Locate every blood parasite and identify its species.
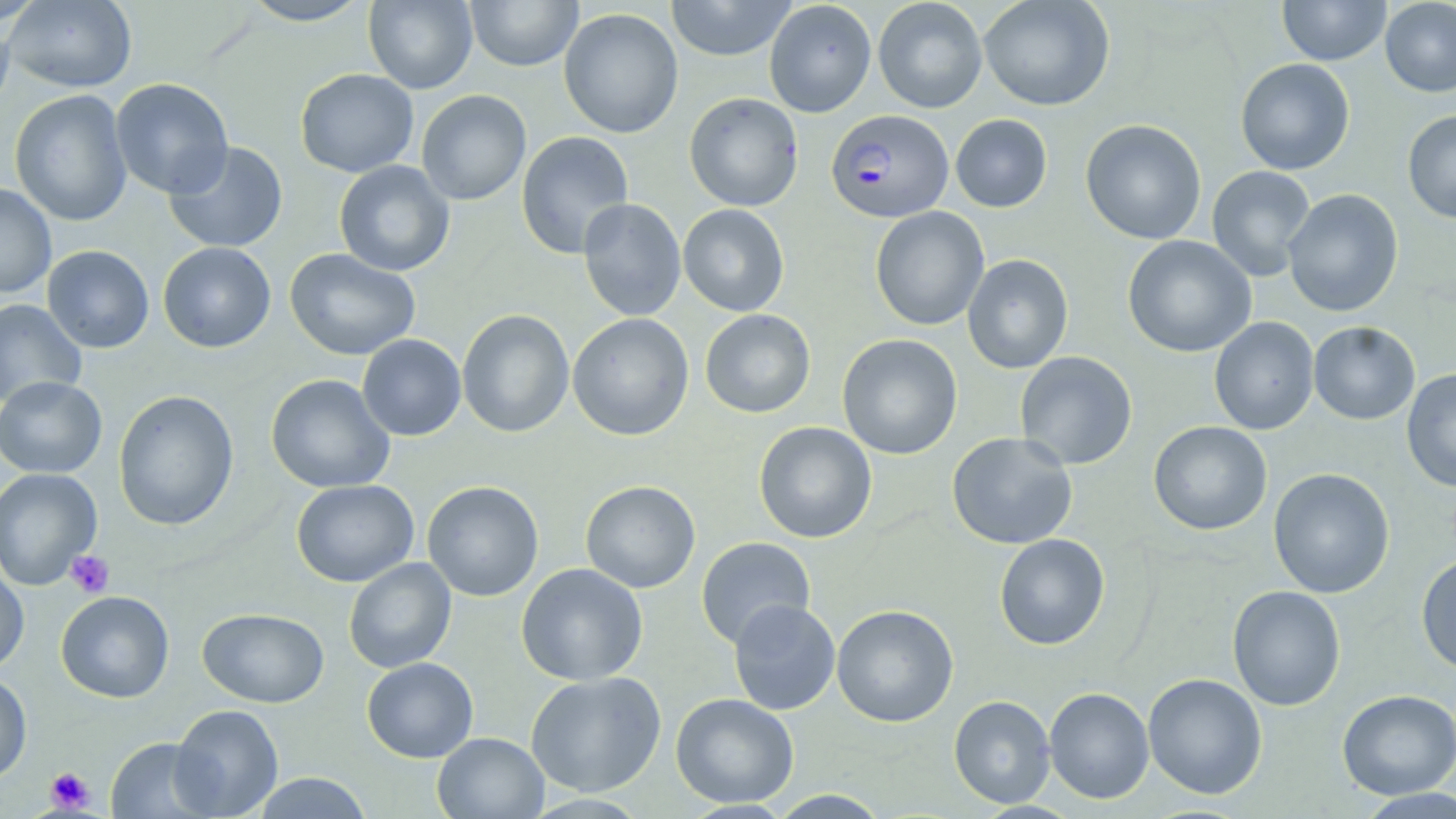

Approximate bounding boxes as named x1/y1/x2/y2 corners in pixels.
Plasmodium falciparum-infected red blood cells: (x1=825, y1=110, x2=953, y2=223).
No Plasmodium ovale, Plasmodium malariae, Plasmodium vivax, Babesia divergens, or Trypanosoma brucei observed.

Platelet locations: (x1=65, y1=550, x2=114, y2=598), (x1=45, y1=766, x2=95, y2=812). Uninfected red blood cell locations: (x1=3, y1=0, x2=137, y2=93), (x1=238, y1=0, x2=373, y2=26), (x1=465, y1=0, x2=583, y2=72), (x1=665, y1=0, x2=798, y2=61), (x1=764, y1=0, x2=877, y2=117), (x1=873, y1=0, x2=988, y2=113), (x1=978, y1=0, x2=1115, y2=111), (x1=1278, y1=0, x2=1391, y2=66), (x1=1380, y1=0, x2=1456, y2=97), (x1=0, y1=1, x2=47, y2=27), (x1=363, y1=1, x2=478, y2=94), (x1=558, y1=8, x2=684, y2=139), (x1=0, y1=13, x2=15, y2=123), (x1=1235, y1=58, x2=1355, y2=175), (x1=295, y1=68, x2=419, y2=178), (x1=110, y1=78, x2=234, y2=199), (x1=9, y1=90, x2=132, y2=227), (x1=416, y1=90, x2=531, y2=205), (x1=683, y1=92, x2=803, y2=211), (x1=1402, y1=110, x2=1456, y2=224), (x1=951, y1=114, x2=1052, y2=213), (x1=1080, y1=118, x2=1207, y2=244), (x1=516, y1=131, x2=634, y2=259), (x1=163, y1=140, x2=288, y2=253), (x1=334, y1=160, x2=455, y2=277), (x1=1207, y1=165, x2=1316, y2=281), (x1=0, y1=183, x2=57, y2=299), (x1=1283, y1=188, x2=1404, y2=317), (x1=577, y1=198, x2=687, y2=321), (x1=677, y1=203, x2=789, y2=317), (x1=870, y1=206, x2=989, y2=331), (x1=1122, y1=235, x2=1256, y2=358), (x1=157, y1=242, x2=276, y2=352), (x1=42, y1=245, x2=154, y2=353), (x1=284, y1=248, x2=421, y2=361), (x1=962, y1=254, x2=1073, y2=374), (x1=0, y1=298, x2=87, y2=408), (x1=457, y1=309, x2=575, y2=438), (x1=700, y1=309, x2=815, y2=418), (x1=568, y1=313, x2=694, y2=441), (x1=1209, y1=317, x2=1320, y2=435), (x1=1308, y1=321, x2=1420, y2=424), (x1=357, y1=334, x2=467, y2=441), (x1=836, y1=334, x2=963, y2=459), (x1=1015, y1=351, x2=1138, y2=470), (x1=1402, y1=368, x2=1456, y2=492), (x1=265, y1=373, x2=395, y2=493), (x1=0, y1=376, x2=107, y2=478), (x1=113, y1=390, x2=239, y2=531), (x1=1148, y1=420, x2=1273, y2=536), (x1=753, y1=421, x2=877, y2=543), (x1=947, y1=432, x2=1078, y2=550), (x1=0, y1=467, x2=102, y2=591), (x1=1268, y1=468, x2=1395, y2=598), (x1=291, y1=479, x2=419, y2=587), (x1=580, y1=480, x2=701, y2=593), (x1=422, y1=481, x2=544, y2=601), (x1=994, y1=534, x2=1110, y2=650), (x1=696, y1=536, x2=816, y2=648), (x1=1416, y1=553, x2=1456, y2=674), (x1=343, y1=558, x2=456, y2=673), (x1=0, y1=562, x2=29, y2=675), (x1=516, y1=563, x2=648, y2=686), (x1=1227, y1=585, x2=1346, y2=711), (x1=55, y1=591, x2=174, y2=703), (x1=728, y1=599, x2=841, y2=715), (x1=831, y1=604, x2=959, y2=727), (x1=197, y1=608, x2=329, y2=708), (x1=361, y1=657, x2=478, y2=763), (x1=525, y1=671, x2=667, y2=797), (x1=0, y1=673, x2=33, y2=784), (x1=1142, y1=673, x2=1268, y2=799), (x1=1044, y1=686, x2=1154, y2=803), (x1=1336, y1=689, x2=1456, y2=799), (x1=671, y1=692, x2=799, y2=808), (x1=948, y1=695, x2=1055, y2=808), (x1=169, y1=703, x2=284, y2=818), (x1=432, y1=732, x2=549, y2=818), (x1=105, y1=737, x2=219, y2=818), (x1=252, y1=773, x2=372, y2=818), (x1=1352, y1=788, x2=1456, y2=818), (x1=767, y1=789, x2=892, y2=818). Slide-level diagnosis: Plasmodium falciparum. Thin blood smear. May-Grünwald-Giemsa stain. Image is 1456×819 pixels. Captured at 1000x magnification. Light microscopy. Single field of view.